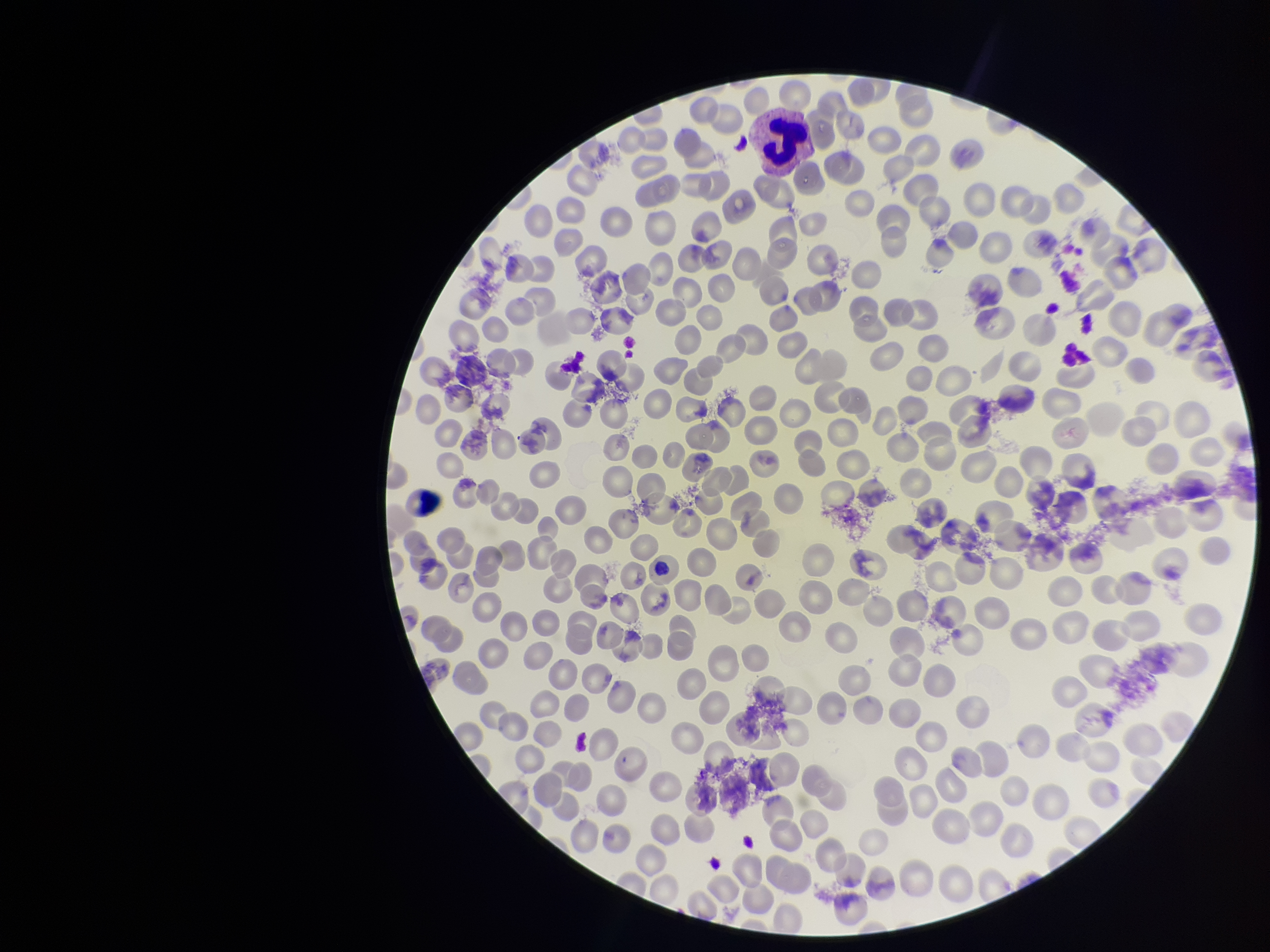 Red blood cell count: 272. Image is 1270×952 pixels. Parasitized red blood cells: none seen. Parasitized red blood cell count: 0. Species reported for this patient: Plasmodium vivax. Patient malaria status: infected. Smartphone photograph taken through the eyepiece of a microscope. Preparation: thin smear. One field from this slide. Stained with Giemsa.